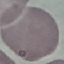
Malaria status: uninfected. Giemsa-stained preparation. Acquired by smartphone through the microscope eyepiece. Thin blood smear. Automatically extracted cell patch, resized to 64 × 64 pixels.